Assess the morphology of the red blood cells.
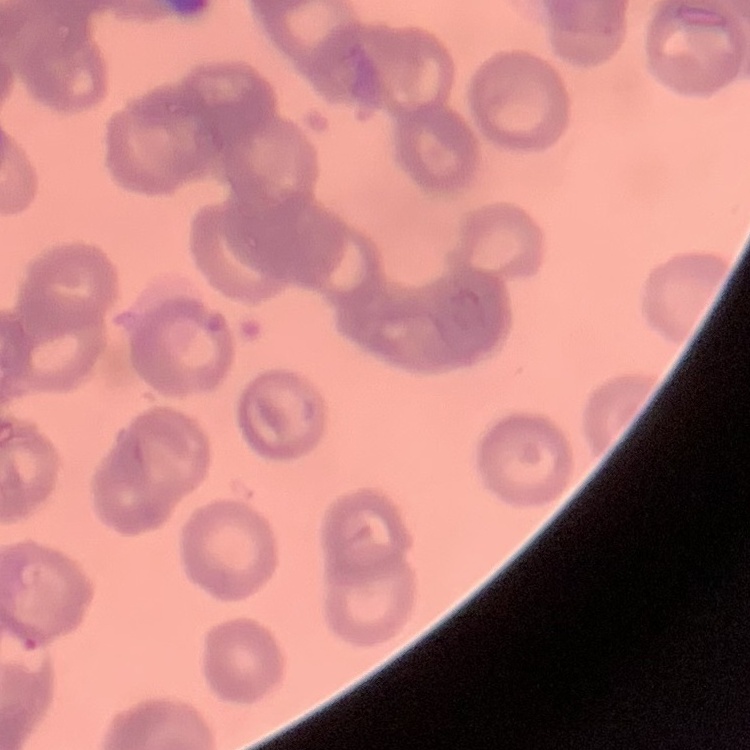

Rouleaux formation.

image type = square crop of a larger photomicrograph
stain = Field's or Giemsa
preparation = thin peripheral smear